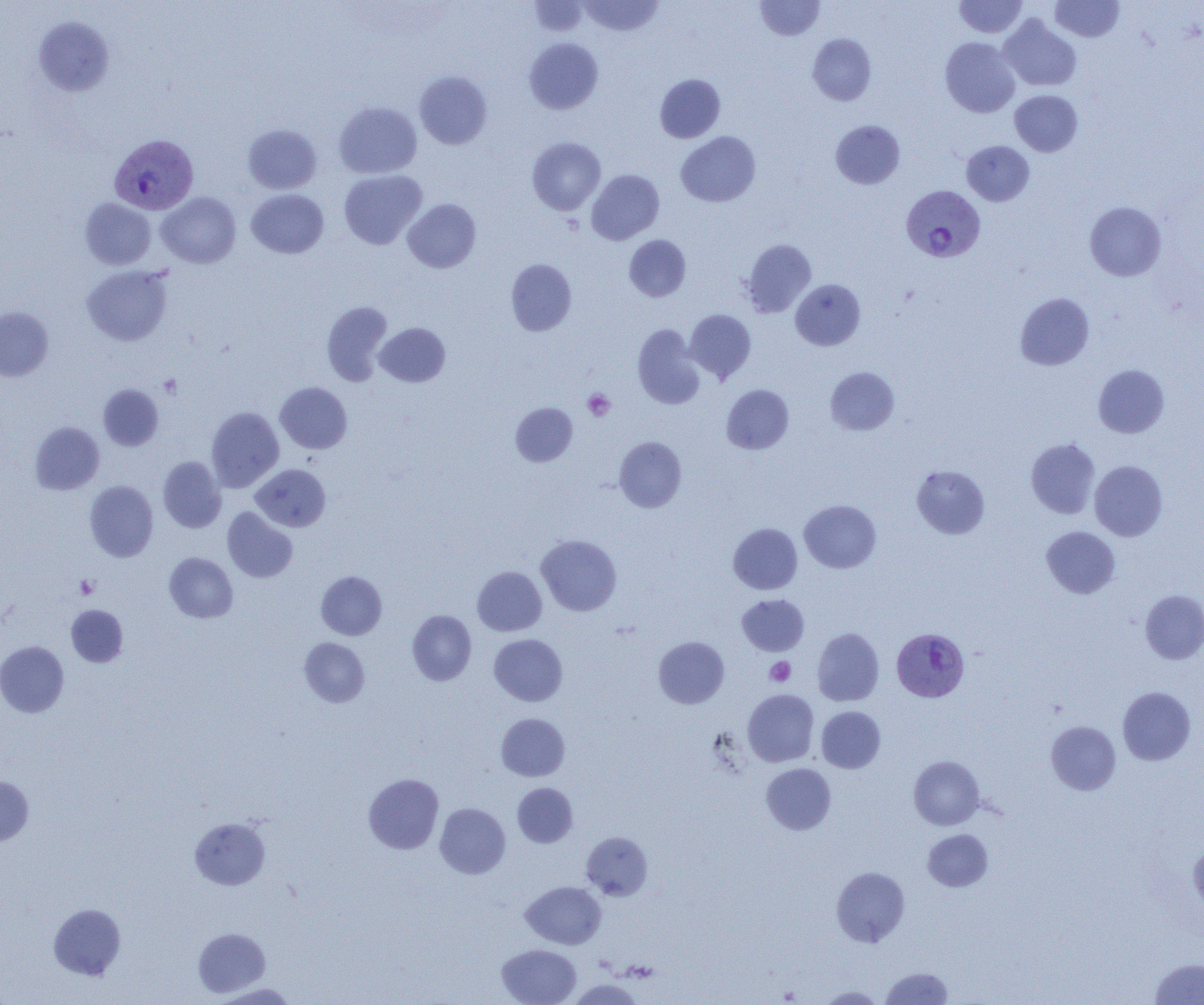
slide-level diagnosis = Plasmodium vivax
preparation = thin blood smear
platelet locations = approximate bounding boxes as (x1, y1, x2, y2) in pixels: (159, 374, 182, 398), (583, 389, 615, 421), (75, 575, 99, 599), (765, 657, 795, 686)
Plasmodium vivax-infected red blood cell locations = approximate bounding boxes as (x1, y1, x2, y2) in pixels: (109, 134, 198, 214), (901, 185, 985, 261), (892, 633, 968, 702)
image size = 1204×1005 pixels
magnification = 1000x
modality = light microscopy
field of view = one of a larger specimen
uninfected red blood cell locations = approximate bounding boxes as (x1, y1, x2, y2) in pixels: (579, 0, 664, 36), (954, 0, 1027, 38), (1050, 0, 1124, 42), (530, 1, 589, 37), (755, 1, 825, 40), (999, 15, 1081, 91), (33, 16, 114, 96), (807, 34, 876, 105), (524, 37, 603, 114), (940, 37, 1019, 117), (414, 71, 492, 149), (655, 74, 725, 143), (1010, 90, 1082, 156), (334, 101, 422, 178), (831, 120, 905, 189), (242, 124, 322, 194), (676, 131, 760, 206), (527, 137, 606, 215), (961, 140, 1034, 206), (339, 170, 427, 249), (586, 170, 664, 244), (246, 189, 328, 258), (157, 192, 241, 268), (80, 198, 156, 270), (403, 199, 481, 272), (1085, 201, 1166, 281), (624, 235, 691, 301), (742, 239, 816, 317), (506, 258, 577, 336), (82, 265, 173, 345), (791, 279, 865, 350), (1015, 293, 1094, 370), (322, 300, 393, 386), (0, 306, 53, 381), (685, 309, 756, 383), (375, 322, 450, 387), (633, 324, 705, 409), (1093, 364, 1169, 438), (825, 367, 900, 435), (275, 382, 352, 453), (98, 384, 163, 450), (721, 384, 794, 454), (510, 403, 577, 466), (206, 406, 284, 491), (30, 421, 104, 494), (614, 437, 687, 512), (1026, 438, 1101, 519), (158, 456, 226, 533), (1090, 460, 1167, 541), (251, 464, 330, 531), (912, 465, 989, 539), (84, 481, 158, 562), (800, 500, 881, 573), (222, 508, 298, 582), (728, 523, 802, 594), (1041, 526, 1120, 598), (536, 535, 621, 616), (164, 553, 238, 623), (472, 566, 546, 636), (316, 571, 387, 640), (1140, 590, 1204, 664), (737, 594, 809, 655), (66, 605, 128, 667), (407, 610, 476, 686), (812, 628, 884, 706), (489, 634, 567, 706), (653, 636, 729, 708), (299, 637, 369, 707), (0, 641, 69, 717), (1118, 687, 1196, 765), (743, 689, 819, 767), (816, 706, 885, 773), (496, 713, 570, 781), (1046, 721, 1121, 795), (909, 756, 984, 830), (761, 763, 836, 835), (363, 773, 443, 854), (0, 776, 33, 845), (512, 783, 578, 847), (435, 803, 510, 878), (190, 817, 270, 889), (922, 829, 993, 891), (581, 831, 652, 900), (1189, 843, 1204, 914), (831, 866, 910, 948), (521, 881, 607, 949), (49, 903, 126, 980), (193, 927, 270, 997), (497, 944, 581, 1005), (1149, 958, 1204, 1004), (880, 967, 953, 1004), (568, 978, 644, 1004), (211, 983, 297, 1004), (817, 986, 886, 1004)